Describe the morphology of the erythrocytes.
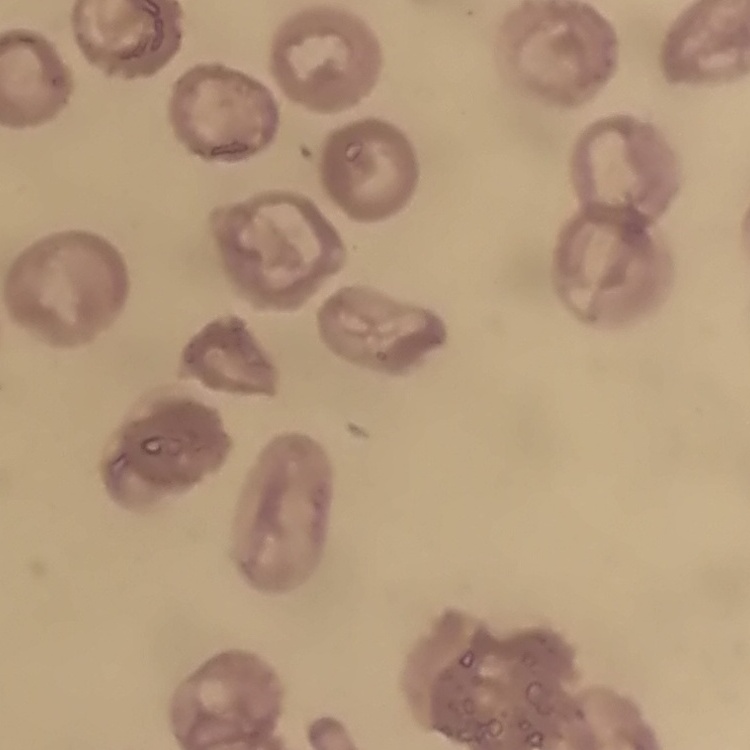

They show no rouleaux formation.

Summary:
  - Preparation: thin peripheral smear
  - Stain: Field's or Giemsa
  - Image type: one tile cut from a larger photomicrograph